Name the cell type shown.
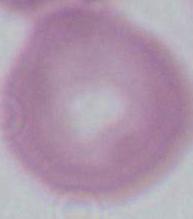

This is an erythrocyte.

Captured at 1000x magnification. Micrograph.